Identify the parasite.
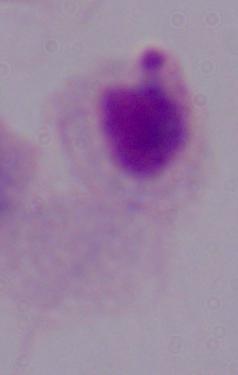
This is a trichomonad.

Summary:
  - Modality: photomicrograph
  - Magnification: 1000x